Locate and identify every blood parasite.
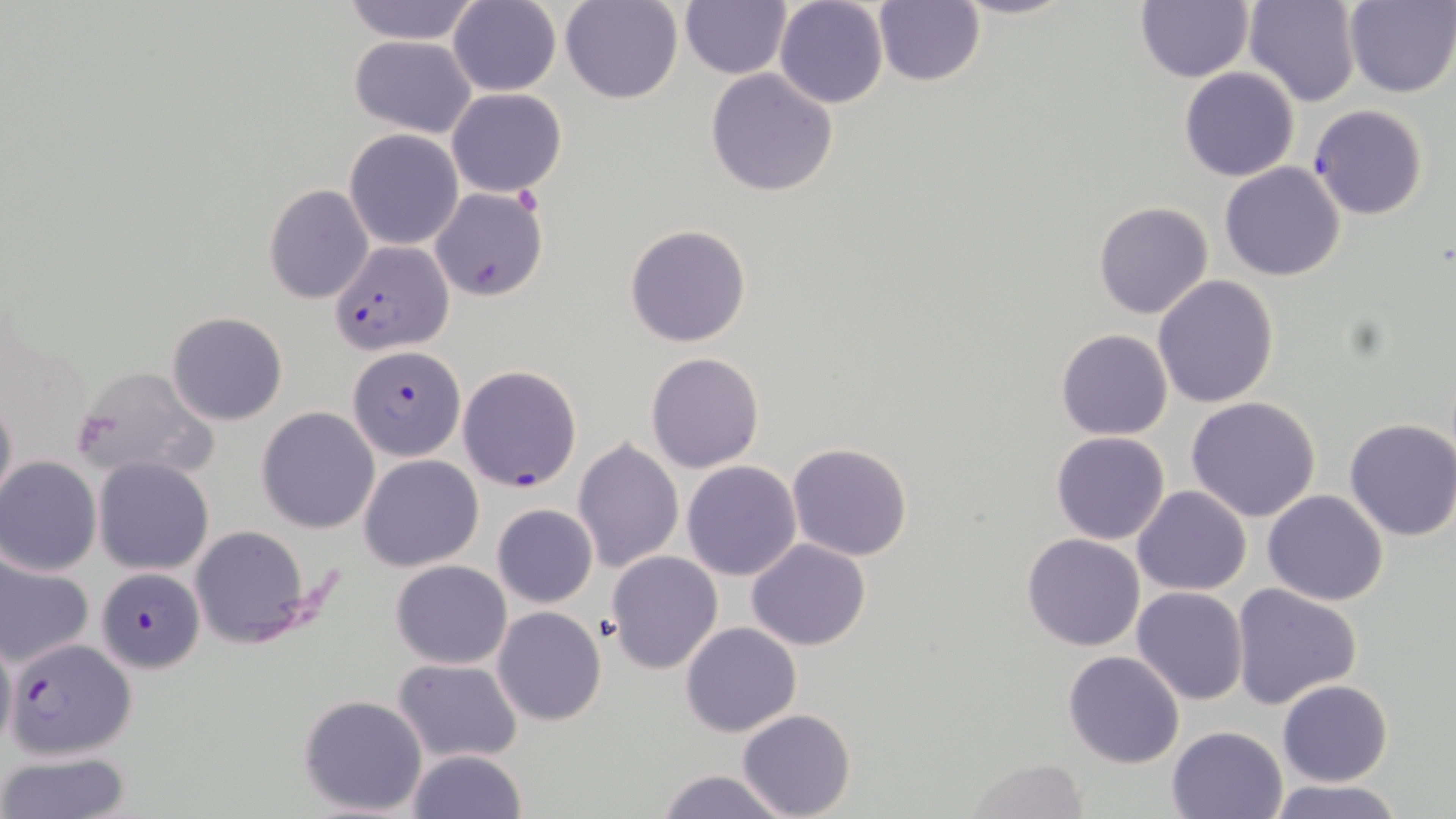

Approximate bounding boxes as [x1, y1, x2, y2] in pixels.
Plasmodium falciparum-infected red blood cells: [1309, 105, 1430, 220], [328, 240, 454, 354], [347, 346, 466, 461], [457, 365, 582, 491], [96, 567, 204, 673], [9, 635, 134, 759].
No Plasmodium ovale, Plasmodium malariae, Plasmodium vivax, Babesia divergens, or Trypanosoma brucei observed.

Summary:
  - Uninfected red blood cell locations: [447, 0, 562, 96], [562, 0, 682, 104], [773, 0, 889, 109], [949, 0, 1077, 20], [1136, 0, 1254, 83], [1243, 0, 1361, 106], [336, 1, 484, 45], [681, 1, 791, 78], [1343, 1, 1455, 97], [871, 2, 986, 87], [349, 34, 476, 136], [1179, 67, 1300, 182], [705, 69, 839, 196], [445, 87, 567, 197], [344, 128, 464, 250], [1218, 160, 1345, 279], [263, 183, 375, 303], [430, 187, 549, 302], [1094, 201, 1212, 320], [624, 224, 752, 347], [1153, 275, 1278, 407], [167, 312, 289, 425], [1055, 328, 1175, 440], [645, 352, 765, 473], [69, 364, 220, 483], [0, 389, 17, 514], [1187, 396, 1321, 521], [257, 406, 381, 532], [1343, 419, 1456, 541], [1051, 431, 1172, 544], [572, 439, 684, 573], [786, 441, 914, 562], [359, 455, 484, 572], [0, 458, 101, 575], [95, 458, 215, 573], [681, 460, 802, 581], [1134, 486, 1252, 597], [1263, 489, 1387, 606], [493, 502, 598, 608], [189, 526, 310, 647], [1021, 532, 1145, 651], [746, 539, 872, 653], [0, 549, 95, 669], [606, 551, 723, 676], [390, 559, 510, 670], [1231, 584, 1363, 709], [1131, 586, 1248, 706], [493, 606, 607, 726], [679, 621, 802, 736], [0, 632, 16, 757], [1062, 650, 1184, 768], [392, 658, 523, 764], [1278, 680, 1392, 786], [298, 694, 428, 816], [738, 709, 856, 819], [1167, 725, 1288, 818], [407, 750, 525, 818], [0, 751, 134, 819], [966, 758, 1091, 818], [656, 770, 791, 819], [1265, 777, 1405, 819]
  - Slide-level diagnosis: Plasmodium falciparum
  - Preparation: thin blood smear
  - Field of view: single
  - Image size: 1456×819 pixels
  - Magnification: 1000x
  - Modality: light microscopy
  - Stain: May-Grünwald-Giemsa